Report the malaria status of this cell.
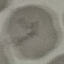

It is uninfected.

Thin blood film. Photographed with a smartphone camera at the microscope eyepiece. Cell patch, automatically extracted from a larger field of view and resized to 64 × 64 pixels. Giemsa stain.